State which parasite is depicted.
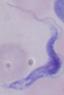
This is a trypanosome.

Summary:
  - Modality: photomicrograph
  - Magnification: 1000x